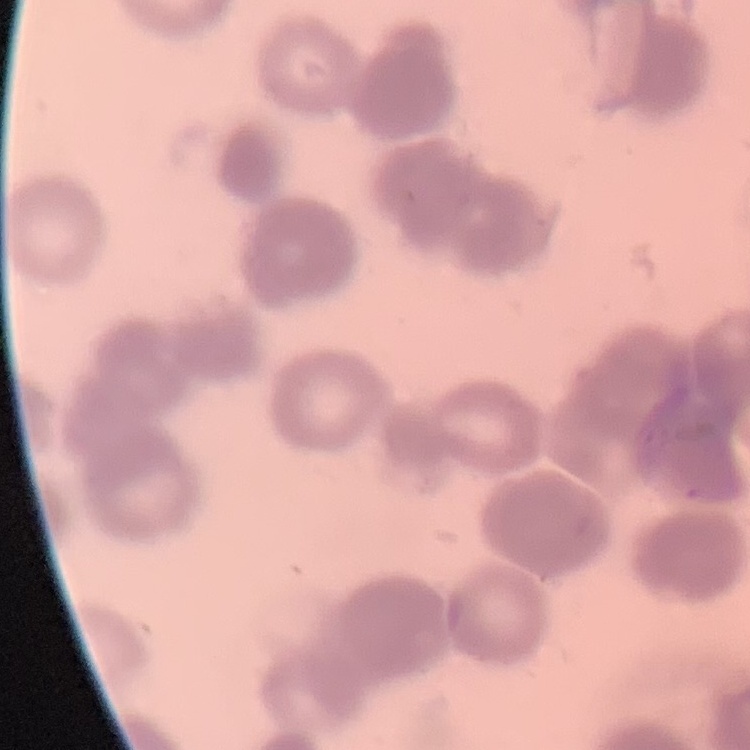

The erythrocytes show rouleaux formation. Thin peripheral smear. One tile cut from a larger photomicrograph. Stained with either Field's or Giemsa.